Assess the morphology of the erythrocytes.
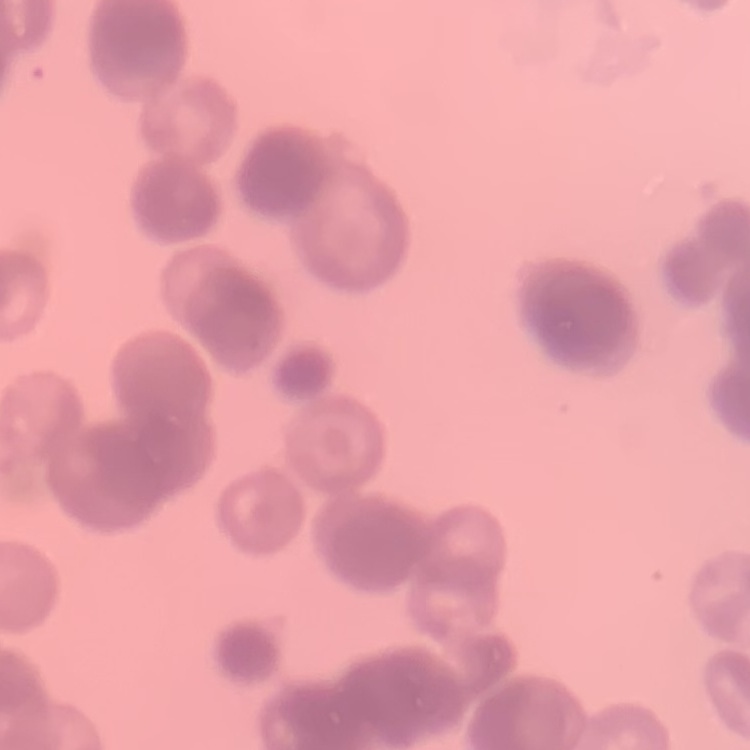

They show rouleaux formation.

{
  "stain": "Field's or Giemsa",
  "preparation": "thin blood smear",
  "image_type": "square crop of a larger photomicrograph"
}